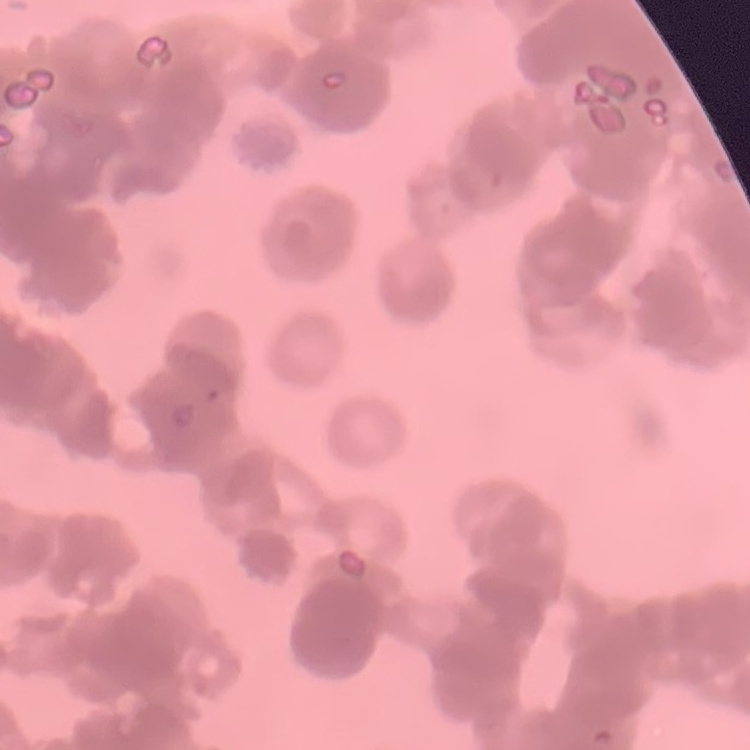

Summary:
  - Erythrocyte morphology: rouleaux formation
  - Image type: one tile cut from a larger photomicrograph
  - Preparation: thin peripheral smear
  - Stain: Field's or Giemsa